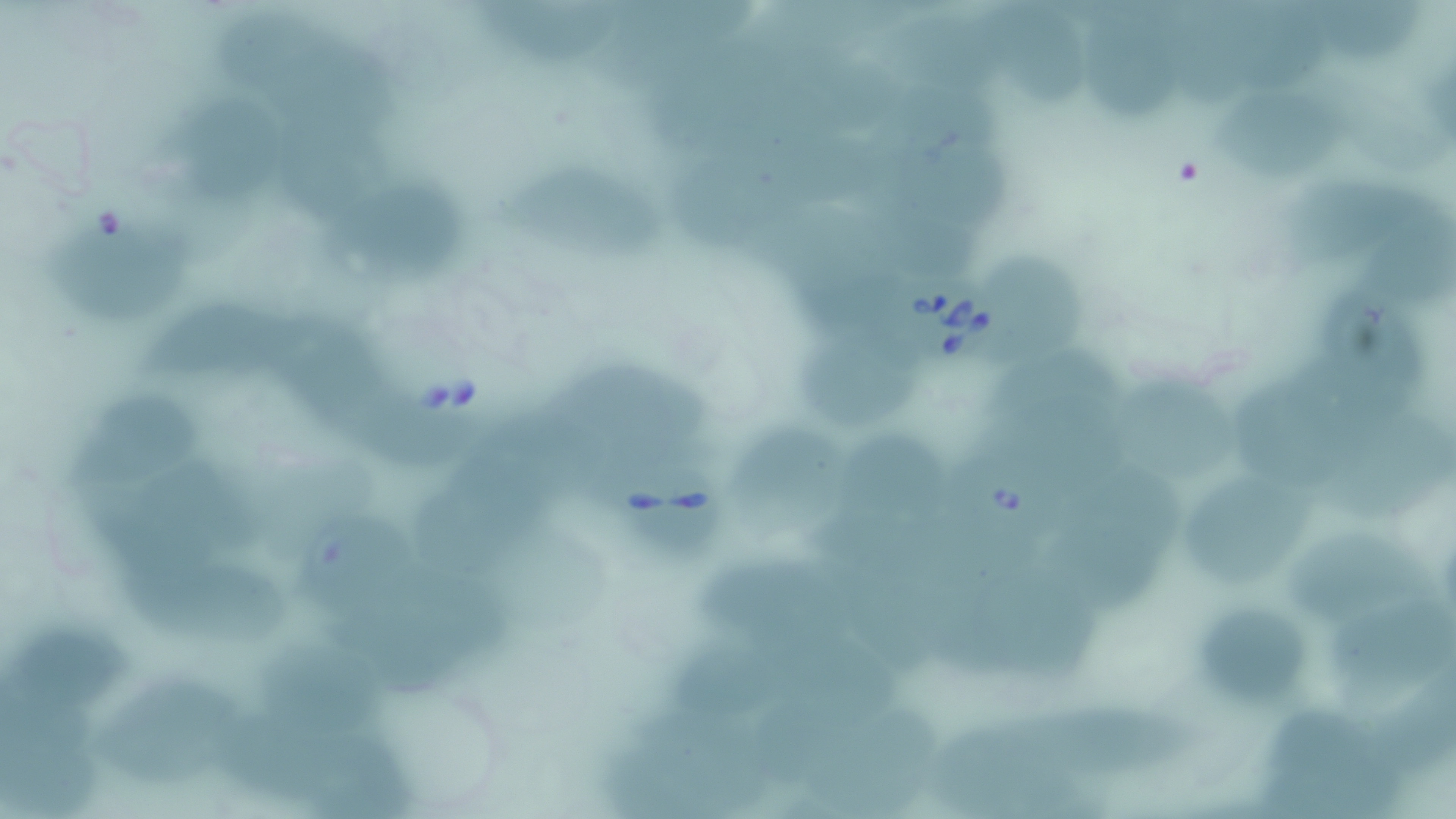

Summary:
  - Coordinate format: approximate bounding boxes as named x1/y1/x2/y2 corners in pixels
  - Uninfected red blood cell locations: (x1=623, y1=5, x2=767, y2=62), (x1=1251, y1=9, x2=1350, y2=90), (x1=975, y1=10, x2=1094, y2=117), (x1=472, y1=11, x2=627, y2=62), (x1=1184, y1=13, x2=1274, y2=105), (x1=1085, y1=15, x2=1188, y2=119), (x1=221, y1=17, x2=339, y2=97), (x1=294, y1=53, x2=405, y2=128), (x1=1228, y1=88, x2=1350, y2=171), (x1=178, y1=97, x2=294, y2=207), (x1=290, y1=121, x2=383, y2=215), (x1=768, y1=135, x2=885, y2=206), (x1=900, y1=136, x2=1023, y2=214), (x1=489, y1=164, x2=674, y2=263), (x1=677, y1=172, x2=820, y2=250), (x1=1288, y1=176, x2=1432, y2=277), (x1=332, y1=195, x2=479, y2=286), (x1=873, y1=207, x2=980, y2=270), (x1=46, y1=216, x2=202, y2=326), (x1=999, y1=250, x2=1089, y2=359), (x1=1345, y1=306, x2=1421, y2=422), (x1=149, y1=309, x2=332, y2=373), (x1=794, y1=310, x2=914, y2=422), (x1=306, y1=328, x2=397, y2=430), (x1=1243, y1=353, x2=1341, y2=469), (x1=989, y1=357, x2=1140, y2=426), (x1=552, y1=364, x2=715, y2=446), (x1=1134, y1=379, x2=1248, y2=467), (x1=64, y1=389, x2=210, y2=501), (x1=363, y1=403, x2=491, y2=475), (x1=458, y1=410, x2=583, y2=494), (x1=743, y1=419, x2=866, y2=532), (x1=1319, y1=421, x2=1452, y2=529), (x1=847, y1=431, x2=941, y2=507), (x1=110, y1=450, x2=272, y2=536), (x1=1058, y1=464, x2=1192, y2=604), (x1=1195, y1=466, x2=1322, y2=578), (x1=436, y1=491, x2=532, y2=566), (x1=315, y1=509, x2=418, y2=608), (x1=810, y1=509, x2=934, y2=557), (x1=1286, y1=529, x2=1422, y2=601), (x1=698, y1=554, x2=842, y2=633), (x1=127, y1=558, x2=295, y2=648), (x1=977, y1=577, x2=1109, y2=680), (x1=343, y1=578, x2=508, y2=679), (x1=1331, y1=592, x2=1456, y2=688), (x1=1207, y1=603, x2=1315, y2=683), (x1=0, y1=620, x2=130, y2=708), (x1=756, y1=620, x2=906, y2=711), (x1=664, y1=636, x2=803, y2=710), (x1=263, y1=639, x2=389, y2=743), (x1=83, y1=684, x2=229, y2=774), (x1=1034, y1=695, x2=1205, y2=767), (x1=759, y1=700, x2=850, y2=777), (x1=814, y1=703, x2=944, y2=802), (x1=1267, y1=703, x2=1397, y2=813), (x1=222, y1=706, x2=367, y2=785), (x1=641, y1=708, x2=791, y2=788), (x1=316, y1=737, x2=421, y2=816)
  - Babesia divergens-infected red blood cell locations: (x1=887, y1=262, x2=1011, y2=369), (x1=941, y1=447, x2=1060, y2=553), (x1=610, y1=456, x2=729, y2=554)
  - Slide-level diagnosis: Babesia divergens
  - Preparation: thin blood smear
  - Modality: optical microscopy
  - Field of view: one of a larger specimen
  - Magnification: 1000x
  - Image size: 1456×819 pixels
  - Stain: May-Grünwald-Giemsa